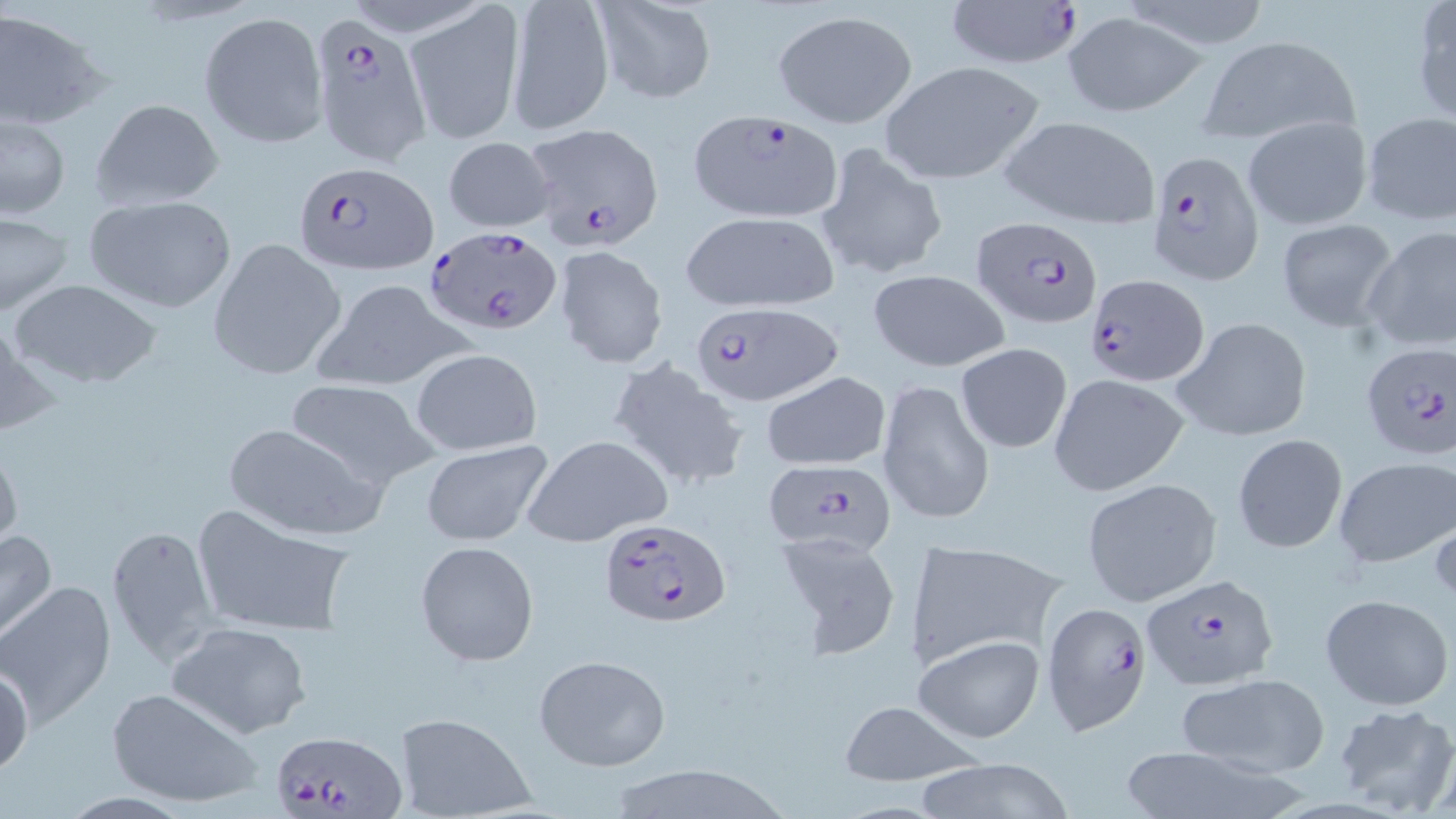
Approximate bounding boxes as named x1/y1/x2/y2 corners in pixels. Uninfected red blood cell locations: (x1=591, y1=0, x2=718, y2=103), (x1=1114, y1=0, x2=1274, y2=52), (x1=505, y1=1, x2=612, y2=133), (x1=1412, y1=1, x2=1456, y2=125), (x1=405, y1=3, x2=525, y2=146), (x1=0, y1=8, x2=108, y2=132), (x1=772, y1=10, x2=915, y2=128), (x1=198, y1=12, x2=328, y2=147), (x1=1062, y1=13, x2=1207, y2=117), (x1=1197, y1=33, x2=1360, y2=146), (x1=878, y1=60, x2=1048, y2=186), (x1=91, y1=99, x2=224, y2=211), (x1=1359, y1=110, x2=1455, y2=226), (x1=1, y1=113, x2=70, y2=220), (x1=1000, y1=115, x2=1162, y2=231), (x1=1242, y1=116, x2=1373, y2=231), (x1=442, y1=137, x2=557, y2=232), (x1=815, y1=142, x2=948, y2=283), (x1=83, y1=195, x2=237, y2=313), (x1=678, y1=209, x2=840, y2=313), (x1=0, y1=212, x2=72, y2=317), (x1=1274, y1=218, x2=1400, y2=331), (x1=1361, y1=224, x2=1456, y2=355), (x1=209, y1=239, x2=347, y2=378), (x1=553, y1=245, x2=668, y2=369), (x1=867, y1=269, x2=1009, y2=373), (x1=9, y1=279, x2=163, y2=388), (x1=311, y1=279, x2=473, y2=395), (x1=1172, y1=315, x2=1313, y2=444), (x1=955, y1=342, x2=1073, y2=454), (x1=412, y1=348, x2=541, y2=456), (x1=608, y1=358, x2=750, y2=491), (x1=761, y1=371, x2=891, y2=471), (x1=1048, y1=373, x2=1190, y2=496), (x1=284, y1=378, x2=439, y2=491), (x1=877, y1=378, x2=996, y2=524), (x1=221, y1=422, x2=383, y2=540), (x1=1232, y1=432, x2=1349, y2=552), (x1=523, y1=434, x2=672, y2=549), (x1=0, y1=440, x2=23, y2=555), (x1=421, y1=440, x2=554, y2=548), (x1=1333, y1=456, x2=1454, y2=569), (x1=1081, y1=479, x2=1220, y2=606), (x1=191, y1=508, x2=357, y2=639), (x1=106, y1=524, x2=217, y2=665), (x1=0, y1=526, x2=57, y2=645), (x1=775, y1=530, x2=905, y2=659), (x1=908, y1=538, x2=1067, y2=668), (x1=415, y1=539, x2=540, y2=667), (x1=1, y1=581, x2=116, y2=728), (x1=1321, y1=594, x2=1452, y2=711), (x1=165, y1=621, x2=312, y2=739), (x1=914, y1=634, x2=1043, y2=743), (x1=533, y1=653, x2=672, y2=772), (x1=0, y1=662, x2=33, y2=778), (x1=1177, y1=673, x2=1330, y2=779), (x1=105, y1=686, x2=263, y2=811), (x1=834, y1=702, x2=985, y2=787), (x1=1331, y1=702, x2=1456, y2=816), (x1=392, y1=713, x2=535, y2=819), (x1=1120, y1=741, x2=1308, y2=819), (x1=914, y1=757, x2=1074, y2=819), (x1=603, y1=764, x2=795, y2=819). Plasmodium falciparum-infected red blood cell locations: (x1=942, y1=0, x2=1083, y2=71), (x1=306, y1=12, x2=432, y2=183), (x1=689, y1=109, x2=845, y2=222), (x1=522, y1=124, x2=664, y2=252), (x1=1148, y1=148, x2=1265, y2=286), (x1=293, y1=159, x2=436, y2=274), (x1=972, y1=215, x2=1101, y2=329), (x1=425, y1=228, x2=564, y2=338), (x1=1086, y1=274, x2=1207, y2=385), (x1=687, y1=302, x2=837, y2=406), (x1=1358, y1=342, x2=1456, y2=464), (x1=759, y1=459, x2=896, y2=557), (x1=596, y1=519, x2=729, y2=630), (x1=1141, y1=574, x2=1279, y2=691), (x1=1040, y1=600, x2=1151, y2=732), (x1=267, y1=730, x2=407, y2=819). Slide-level diagnosis: Plasmodium falciparum. Image is 1456×819 pixels. Thin blood smear. Captured at 1000x magnification. May-Grünwald-Giemsa-stained preparation. Light microscopy. One field of a larger specimen.